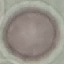

Summary:
  - Malaria status: uninfected
  - Image type: cell patch, automatically extracted from a larger field of view and resized to 64 × 64 pixels
  - Stain: Giemsa
  - Preparation: thin blood smear
  - Capture: smartphone camera at the microscope eyepiece